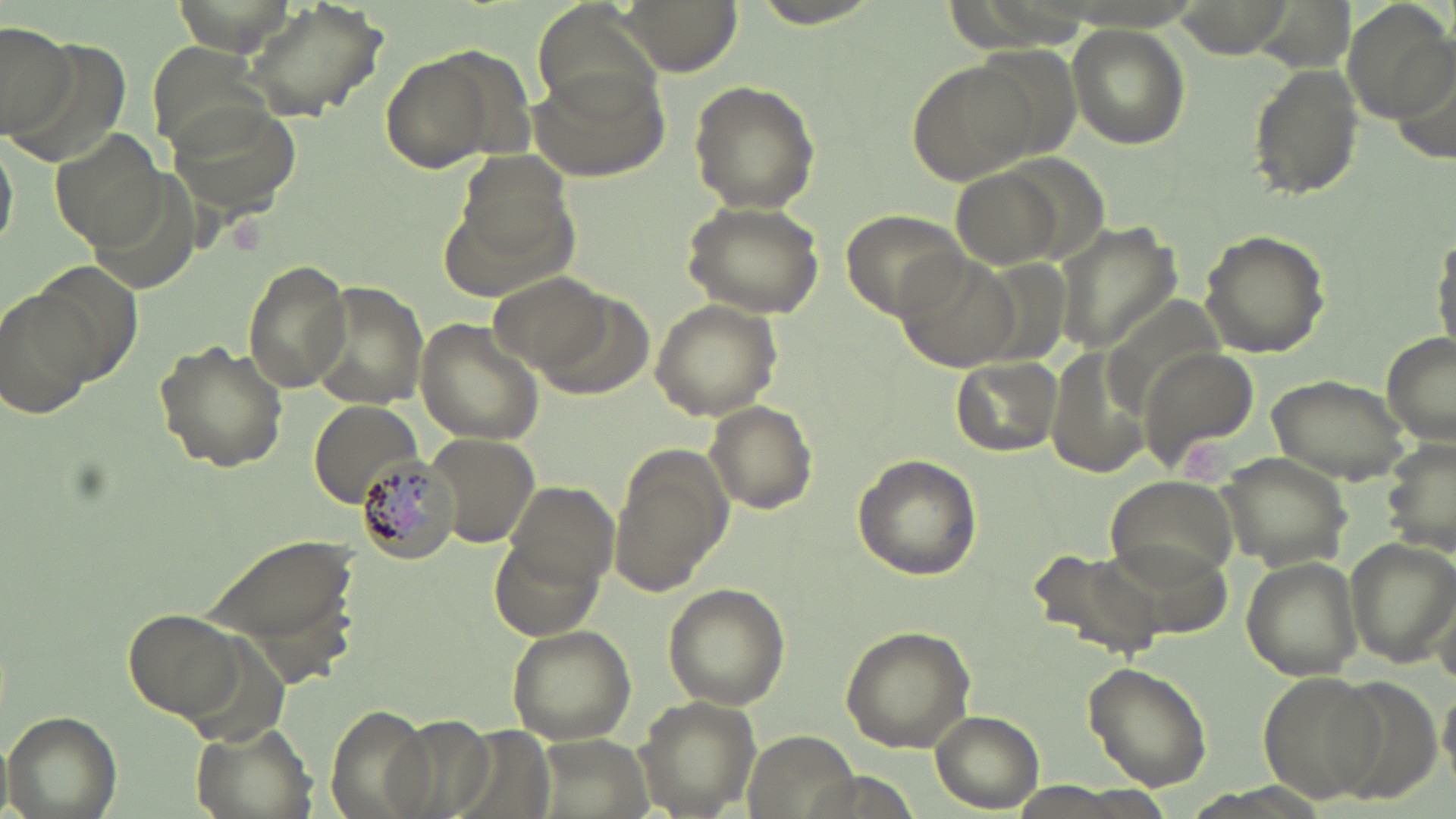

slide-level diagnosis = Plasmodium malariae
modality = optical microscopy
stain = May-Grünwald-Giemsa
preparation = thin blood smear
Plasmodium malariae-infected red blood cell locations = approximate bounding boxes as named x1/y1/x2/y2 corners in pixels: (x1=355, y1=451, x2=462, y2=563)
image size = 1456×819 pixels
uninfected red blood cell locations = approximate bounding boxes as named x1/y1/x2/y2 corners in pixels: (x1=241, y1=0, x2=390, y2=121), (x1=618, y1=0, x2=741, y2=73), (x1=750, y1=0, x2=887, y2=29), (x1=1345, y1=2, x2=1454, y2=119), (x1=1065, y1=21, x2=1191, y2=148), (x1=0, y1=24, x2=76, y2=142), (x1=377, y1=45, x2=513, y2=175), (x1=1387, y1=45, x2=1456, y2=173), (x1=906, y1=60, x2=1034, y2=187), (x1=1247, y1=62, x2=1366, y2=200), (x1=525, y1=63, x2=670, y2=183), (x1=689, y1=81, x2=822, y2=214), (x1=166, y1=96, x2=302, y2=217), (x1=47, y1=129, x2=170, y2=249), (x1=0, y1=132, x2=17, y2=257), (x1=951, y1=167, x2=1062, y2=267), (x1=681, y1=199, x2=825, y2=319), (x1=840, y1=206, x2=972, y2=321), (x1=1056, y1=223, x2=1182, y2=355), (x1=1198, y1=228, x2=1331, y2=359), (x1=1433, y1=242, x2=1456, y2=354), (x1=895, y1=251, x2=1019, y2=368), (x1=242, y1=257, x2=353, y2=393), (x1=26, y1=261, x2=140, y2=384), (x1=487, y1=271, x2=614, y2=379), (x1=307, y1=282, x2=429, y2=407), (x1=2, y1=285, x2=104, y2=421), (x1=648, y1=299, x2=782, y2=421), (x1=415, y1=317, x2=546, y2=445), (x1=1381, y1=331, x2=1456, y2=445), (x1=151, y1=339, x2=289, y2=473), (x1=1142, y1=345, x2=1258, y2=472), (x1=1044, y1=348, x2=1154, y2=485), (x1=951, y1=356, x2=1062, y2=458), (x1=1266, y1=372, x2=1414, y2=484), (x1=305, y1=398, x2=423, y2=510), (x1=704, y1=399, x2=820, y2=513), (x1=424, y1=431, x2=542, y2=548), (x1=1388, y1=437, x2=1455, y2=555), (x1=608, y1=443, x2=732, y2=598), (x1=1217, y1=453, x2=1355, y2=568), (x1=851, y1=454, x2=982, y2=580), (x1=1104, y1=475, x2=1245, y2=587), (x1=503, y1=481, x2=619, y2=588), (x1=200, y1=528, x2=362, y2=675), (x1=487, y1=533, x2=604, y2=640), (x1=1342, y1=535, x2=1456, y2=669), (x1=1026, y1=547, x2=1163, y2=661), (x1=1242, y1=556, x2=1363, y2=677), (x1=661, y1=583, x2=790, y2=708), (x1=120, y1=606, x2=246, y2=721), (x1=506, y1=624, x2=636, y2=744), (x1=839, y1=625, x2=977, y2=755), (x1=1082, y1=661, x2=1214, y2=792), (x1=1258, y1=671, x2=1385, y2=801), (x1=636, y1=696, x2=762, y2=818), (x1=324, y1=703, x2=437, y2=819), (x1=4, y1=709, x2=122, y2=819), (x1=930, y1=710, x2=1043, y2=812), (x1=186, y1=721, x2=316, y2=819)
field of view = one of a larger specimen
magnification = 1000x